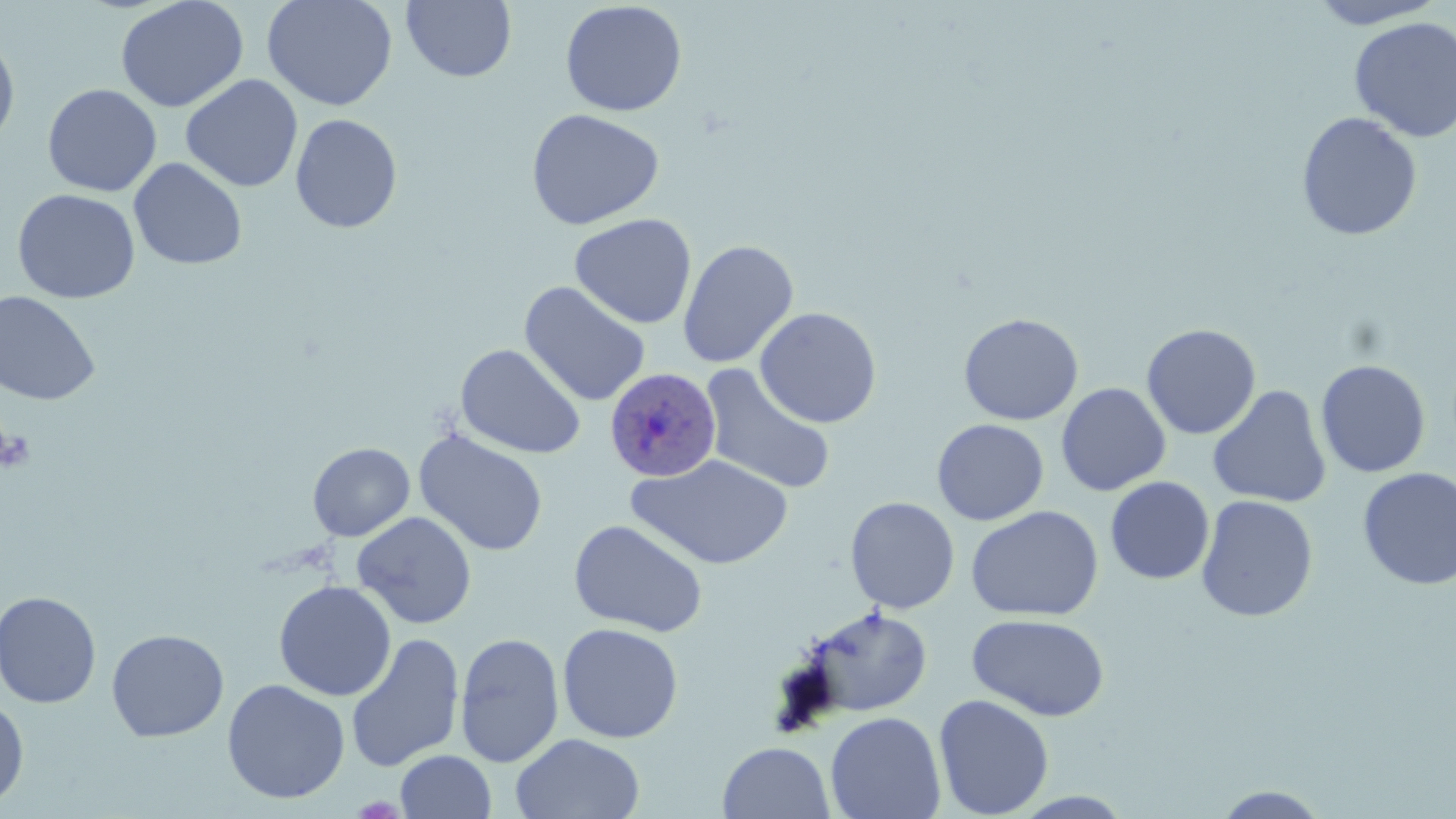

Approximate bounding boxes as (x1, y1, x2, y2) in pixels. Uninfected red blood cell locations: (115, 0, 249, 113), (261, 0, 398, 111), (1306, 0, 1449, 29), (402, 1, 516, 83), (559, 1, 687, 117), (1348, 17, 1456, 143), (0, 34, 20, 149), (180, 74, 303, 192), (42, 83, 162, 197), (526, 108, 665, 231), (1296, 111, 1423, 241), (290, 114, 403, 233), (128, 157, 248, 270), (12, 188, 140, 304), (569, 213, 697, 329), (678, 239, 799, 368), (518, 281, 651, 407), (0, 290, 101, 406), (754, 306, 882, 429), (959, 313, 1084, 426), (1141, 323, 1261, 440), (455, 343, 586, 460), (1315, 359, 1431, 478), (700, 364, 836, 495), (1056, 383, 1171, 496), (1207, 385, 1332, 508), (931, 419, 1049, 525), (413, 428, 549, 557), (307, 442, 415, 541), (628, 454, 795, 570), (1356, 467, 1456, 590), (1105, 477, 1215, 584), (1196, 495, 1318, 622), (845, 496, 960, 614), (966, 505, 1104, 622), (352, 511, 477, 629), (568, 519, 709, 637), (273, 580, 396, 701), (0, 590, 102, 708), (798, 606, 933, 718), (967, 613, 1111, 721), (557, 623, 684, 743), (106, 628, 229, 742), (345, 632, 465, 773), (454, 632, 564, 767), (222, 678, 350, 804), (933, 694, 1054, 818), (0, 696, 29, 810), (825, 711, 946, 819), (511, 733, 645, 819), (717, 741, 836, 819), (395, 750, 496, 819), (1212, 785, 1331, 818). Plasmodium ovale-infected red blood cell locations: (604, 365, 723, 483). Platelet locations: (0, 427, 35, 472). Slide-level diagnosis: Plasmodium ovale. May-Grünwald-Giemsa stain. Light microscopy. Captured at 1000x magnification. Image is 1456×819 pixels. Thin blood smear. Single field of view.